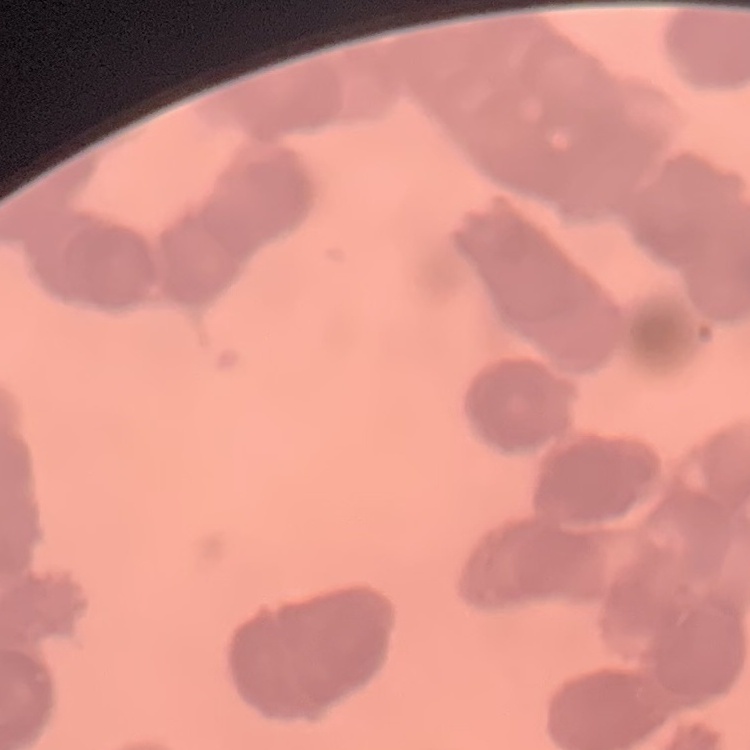

The red blood cells show rouleaux formation. Square crop of a larger photomicrograph. Thin blood film. Stained with either Field's or Giemsa.